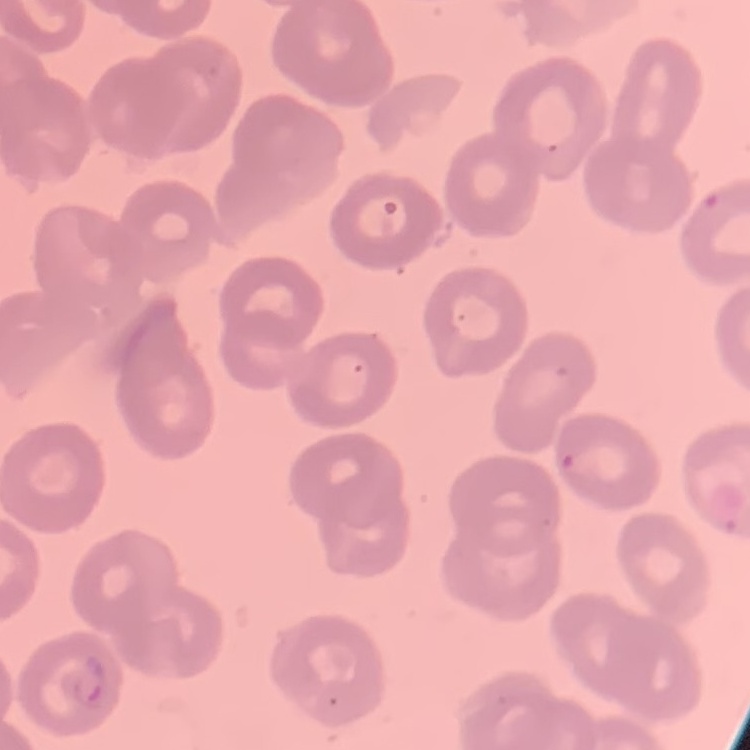

erythrocyte morphology = no rouleaux formation
preparation = thin blood smear
stain = Field's or Giemsa
image type = square crop of a larger photomicrograph